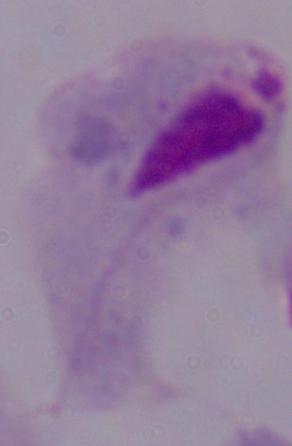

Summary:
  - Modality: photomicrograph
  - Identification: trichomonad
  - Magnification: 1000x